State which parasite is depicted.
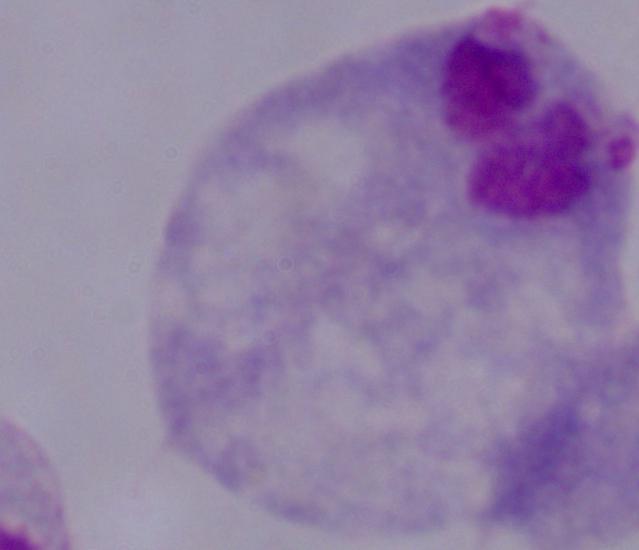

This is a trichomonad.

magnification: 1000x
modality: photomicrograph